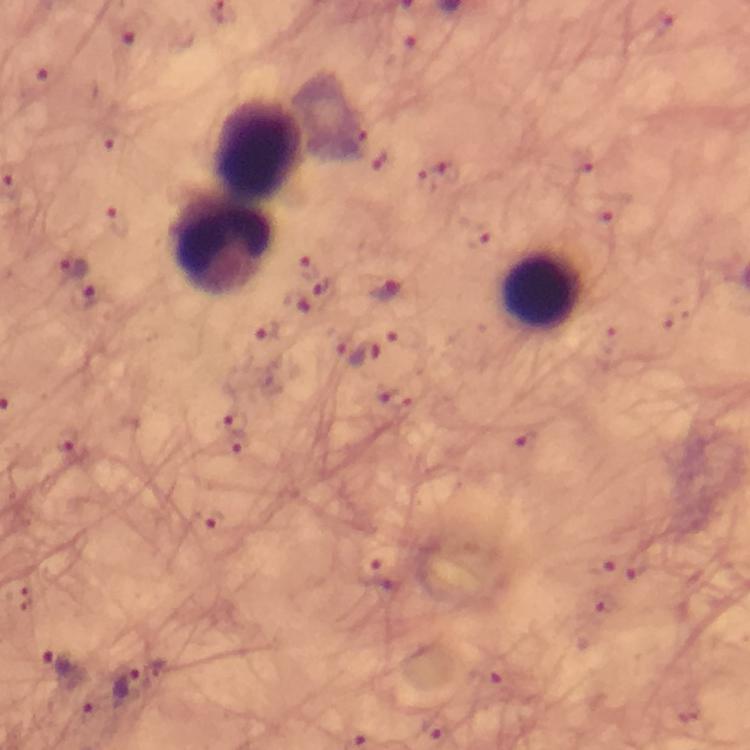

Approximate centers as (x, y) in pixels.
Summary:
  - Plasmodium parasite locations: (133, 31), (41, 81), (439, 174), (605, 219), (118, 223), (478, 236), (74, 267), (307, 267), (325, 290), (388, 293), (84, 298), (296, 301), (266, 331), (364, 356), (394, 400), (237, 423), (524, 438), (67, 439), (238, 444), (213, 523), (638, 564), (601, 566), (366, 568), (602, 602), (60, 664), (494, 673), (127, 686), (436, 728)
  - Leukocyte locations: (261, 146), (222, 246), (543, 290)
  - Stain: Giemsa
  - Context: from a malaria diagnostic workup
  - Image size: 750×750 pixels
  - Capture: smartphone camera through the microscope
  - Immersion oil: used
  - Cropped from: a single field of view
  - Preparation: thick blood smear
  - Magnification: 100x